Assess this cell for malaria.
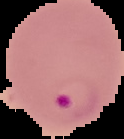

It is parasitized.

Summary:
  - Image type: segmented cell region with the area outside set to black
  - Image size: 124×139 pixels
  - Preparation: thin blood smear